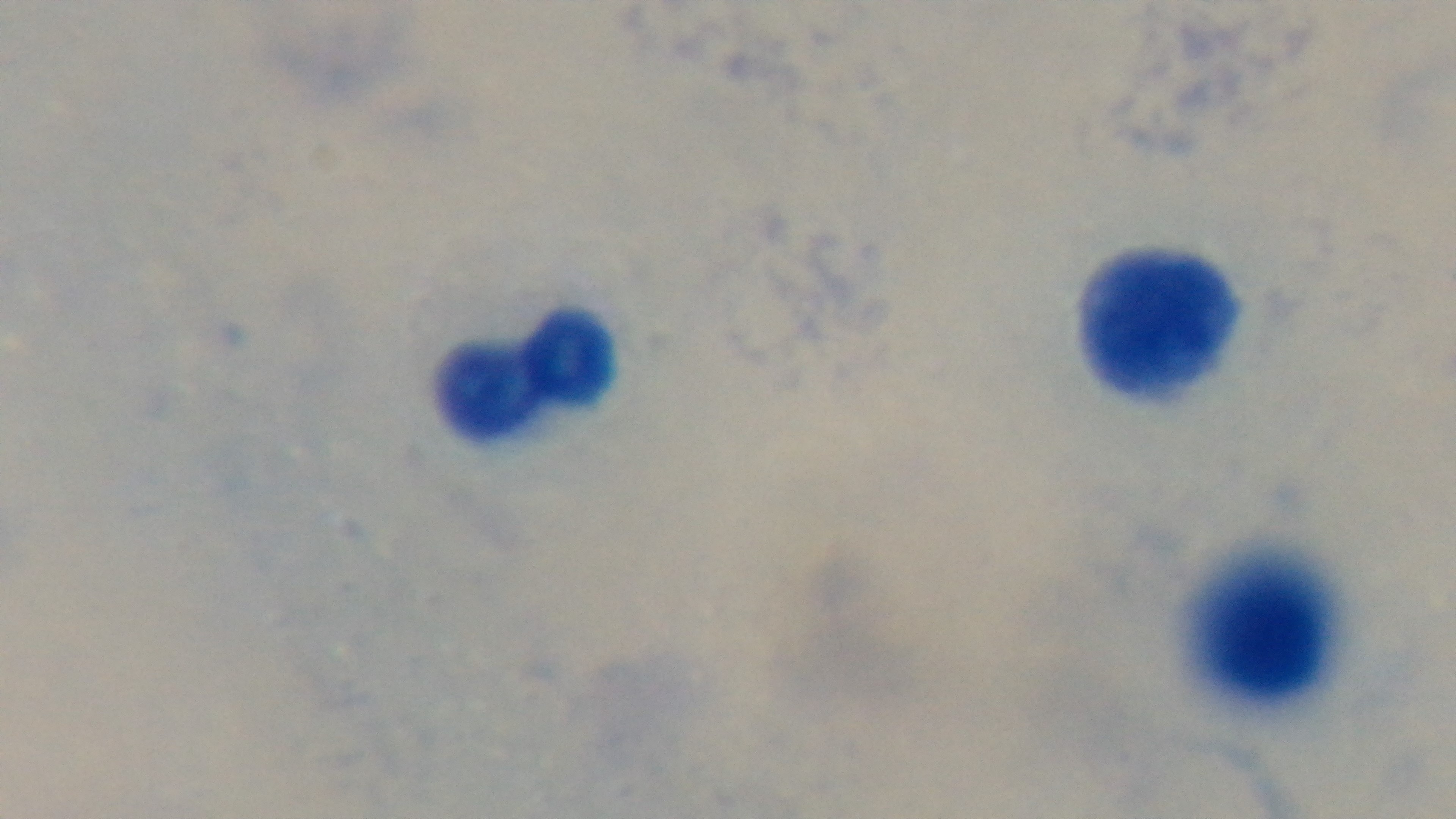
{
  "field_of_view": "one from the slide",
  "preparation": "thick",
  "stain": "Giemsa",
  "malaria_status": "negative",
  "modality": "light microscopy",
  "objective": "100x oil immersion",
  "capture": "mounted 4K digital camera"
}